Name the parasite shown.
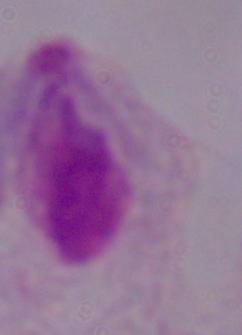
This is a trichomonad.

Photomicrograph. 1000x magnification.